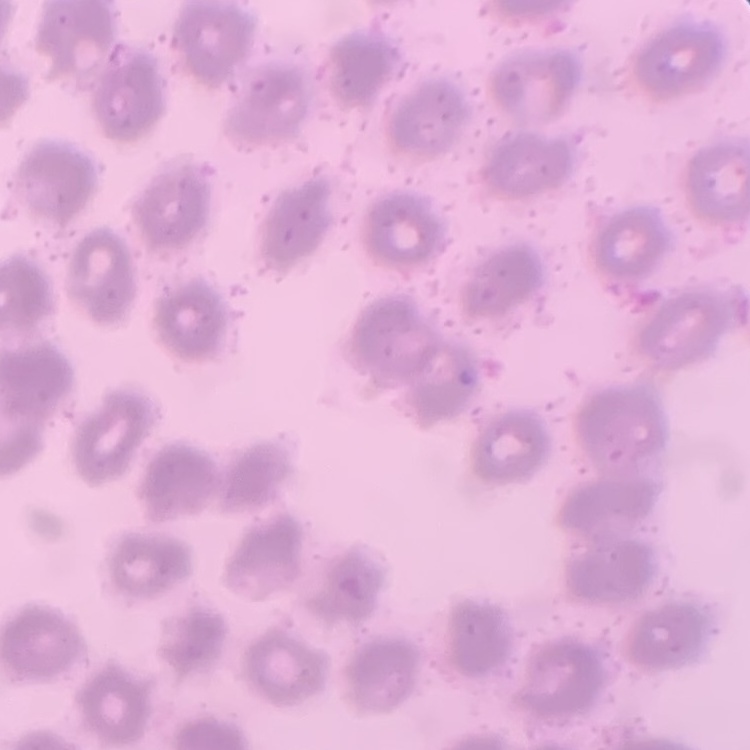
The erythrocytes show no rouleaux formation. Thin peripheral smear. Square crop of a larger photomicrograph. Stained with either Field's or Giemsa.